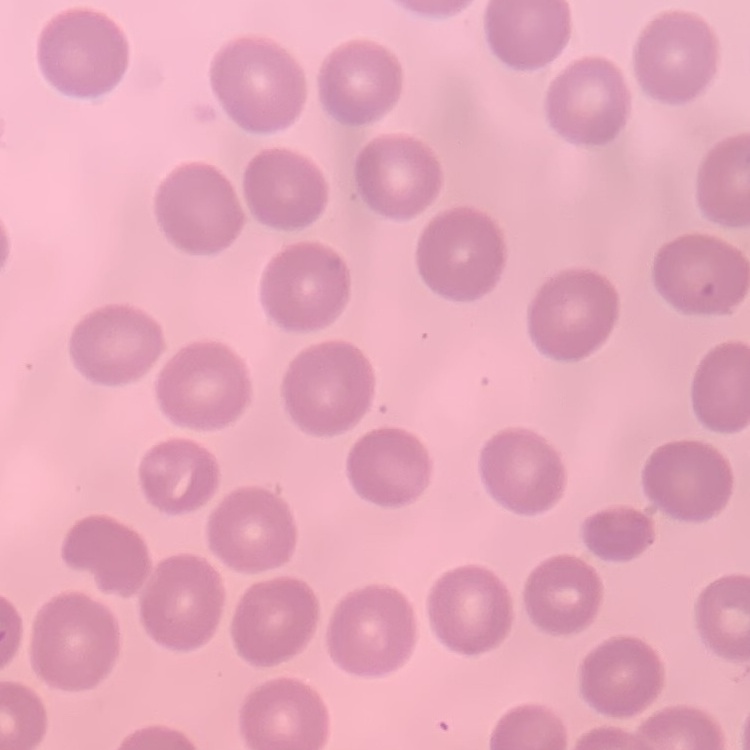

red blood cell morphology = no rouleaux formation
image type = one tile cut from a larger photomicrograph
preparation = thin peripheral smear
stain = Field's or Giemsa